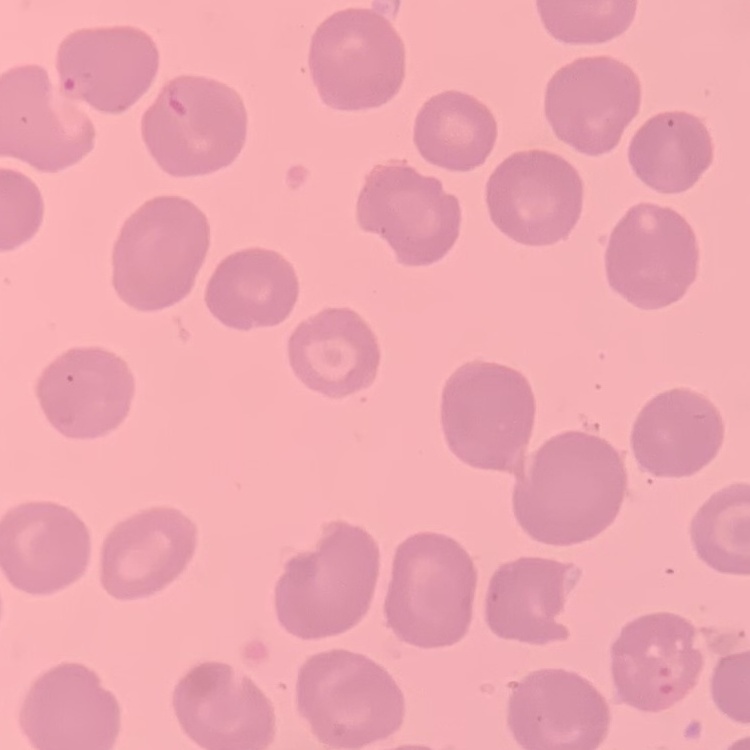
{
  "red_blood_cell_morphology": "no rouleaux formation",
  "image_type": "square crop of a larger photomicrograph",
  "stain": "Field's or Giemsa",
  "preparation": "thin blood smear"
}